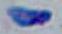 1000x magnification. Micrograph. Toxoplasma gondii is shown.